Assess this cell for malaria.
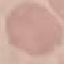

Uninfected.

Summary:
  - Image type: cell patch, automatically extracted from a larger field of view and resized to 64 × 64 pixels
  - Preparation: thin blood smear
  - Capture: smartphone camera at the microscope eyepiece
  - Stain: Giemsa